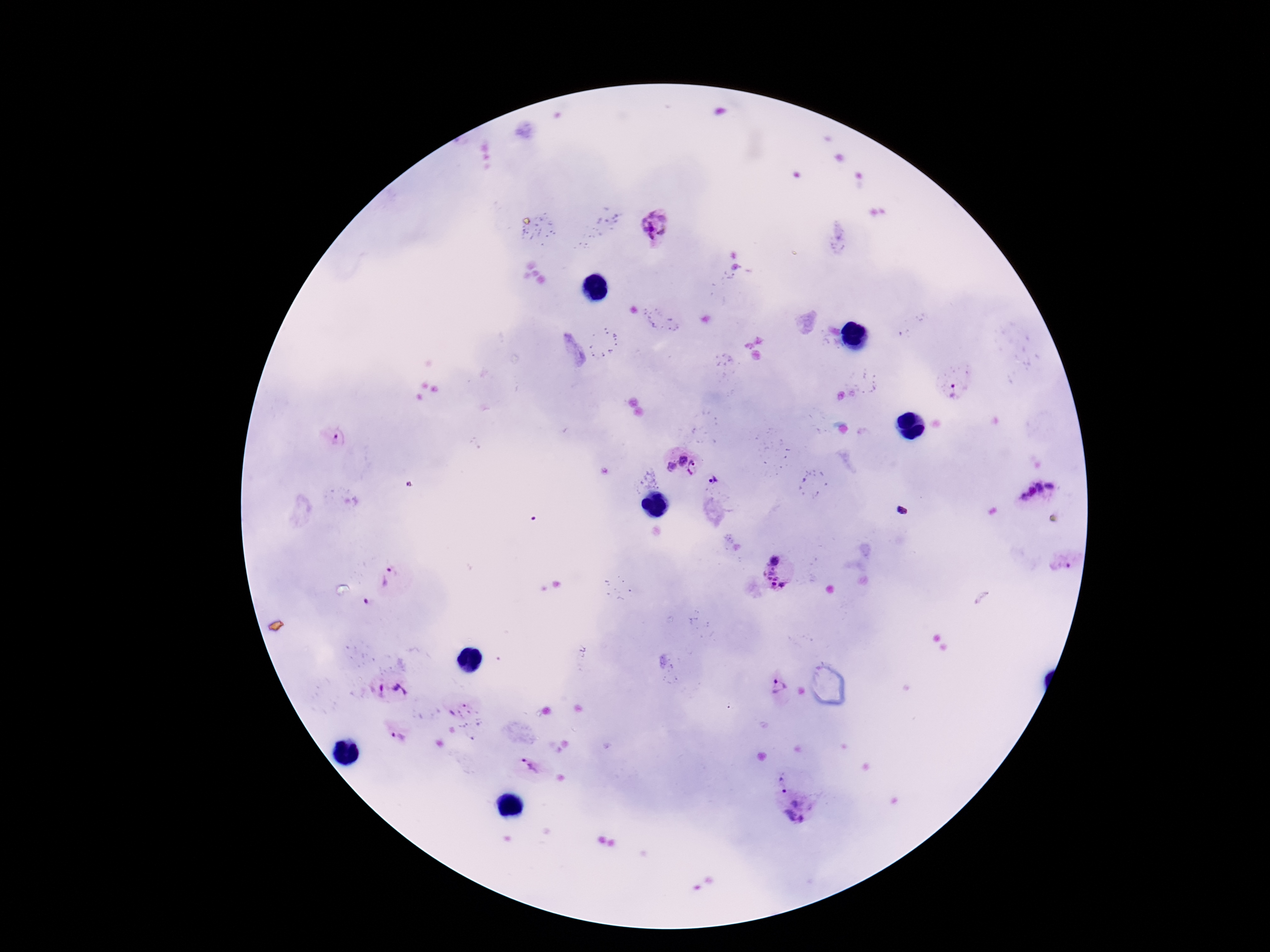

Approximate object centers, in pixels from the top-left corner. Plasmodium parasite locations: (x=655, y=226), (x=954, y=388), (x=337, y=439), (x=682, y=461), (x=671, y=468), (x=695, y=468), (x=713, y=482), (x=1049, y=486), (x=1040, y=489), (x=1030, y=492), (x=1024, y=498), (x=774, y=559), (x=1062, y=565), (x=389, y=579), (x=775, y=580), (x=368, y=603), (x=778, y=688), (x=392, y=693), (x=456, y=706), (x=399, y=738), (x=530, y=769), (x=782, y=785), (x=798, y=815). Smartphone photograph taken through the microscope eyepiece. Patient malaria status: positive. Giemsa stain. Image is 1270×952 pixels. Single field of view. 100x magnification. Thick peripheral-blood smear.